Assess the morphology of the red blood cells.
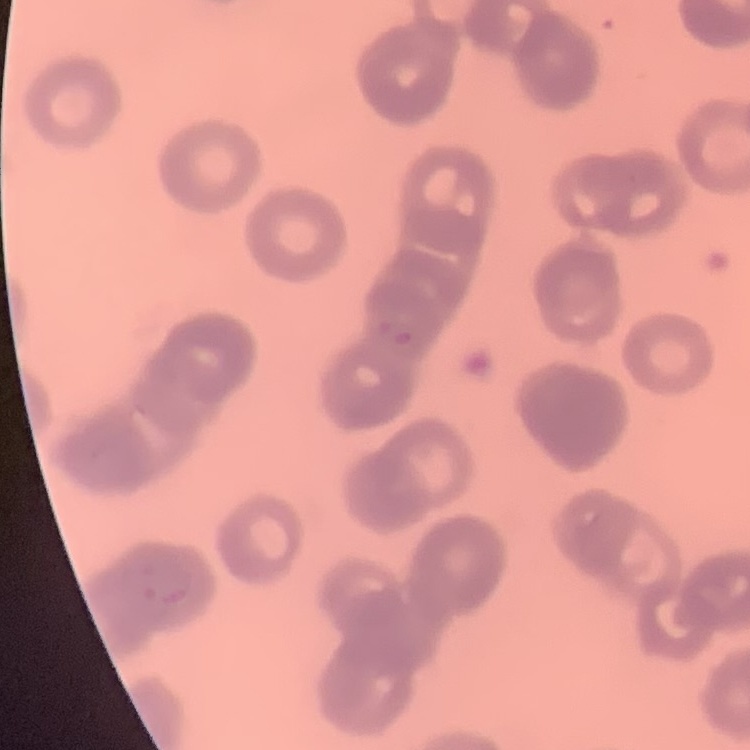
They show rouleaux formation.

{
  "image_type": "one tile cut from a larger photomicrograph",
  "stain": "Field's or Giemsa",
  "preparation": "thin blood film"
}